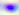
magnification = 400x
modality = photomicrograph
identification = Toxoplasma gondii